Classify this cell by malaria status.
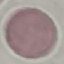
Uninfected.

Summary:
  - Image type: automatically extracted cell patch, resized to 64 × 64 pixels
  - Capture: smartphone through the microscope eyepiece
  - Stain: Giemsa
  - Preparation: thin blood film